Classify this cell by malaria status.
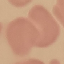
It is uninfected.

Thin smear of blood. Acquired by smartphone through the microscope eyepiece. Cell patch, automatically extracted from a larger field of view and resized to 64 × 64 pixels. Giemsa-stained preparation.